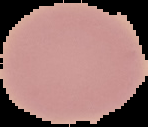

{
  "image_type": "segmented cell region with the area outside set to black",
  "preparation": "thin blood smear",
  "malaria_status": "uninfected",
  "image_size": "148×127 pixels"
}